Report the malaria status of this cell.
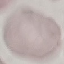
It is uninfected.

Summary:
  - Preparation: thin smear
  - Image type: cell patch, automatically extracted from a larger field of view and resized to 64 × 64 pixels
  - Stain: Giemsa
  - Capture: smartphone through the microscope eyepiece